Identify the cell.
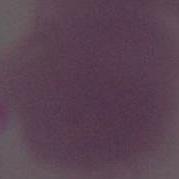
This is an erythrocyte.

Micrograph. Captured at 1000x magnification.